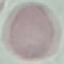
malaria status = uninfected
stain = Giemsa
capture = smartphone camera at the microscope eyepiece
image type = cell patch, automatically extracted from a larger field of view and resized to 64 × 64 pixels
preparation = thin smear